Mark where platelets are.
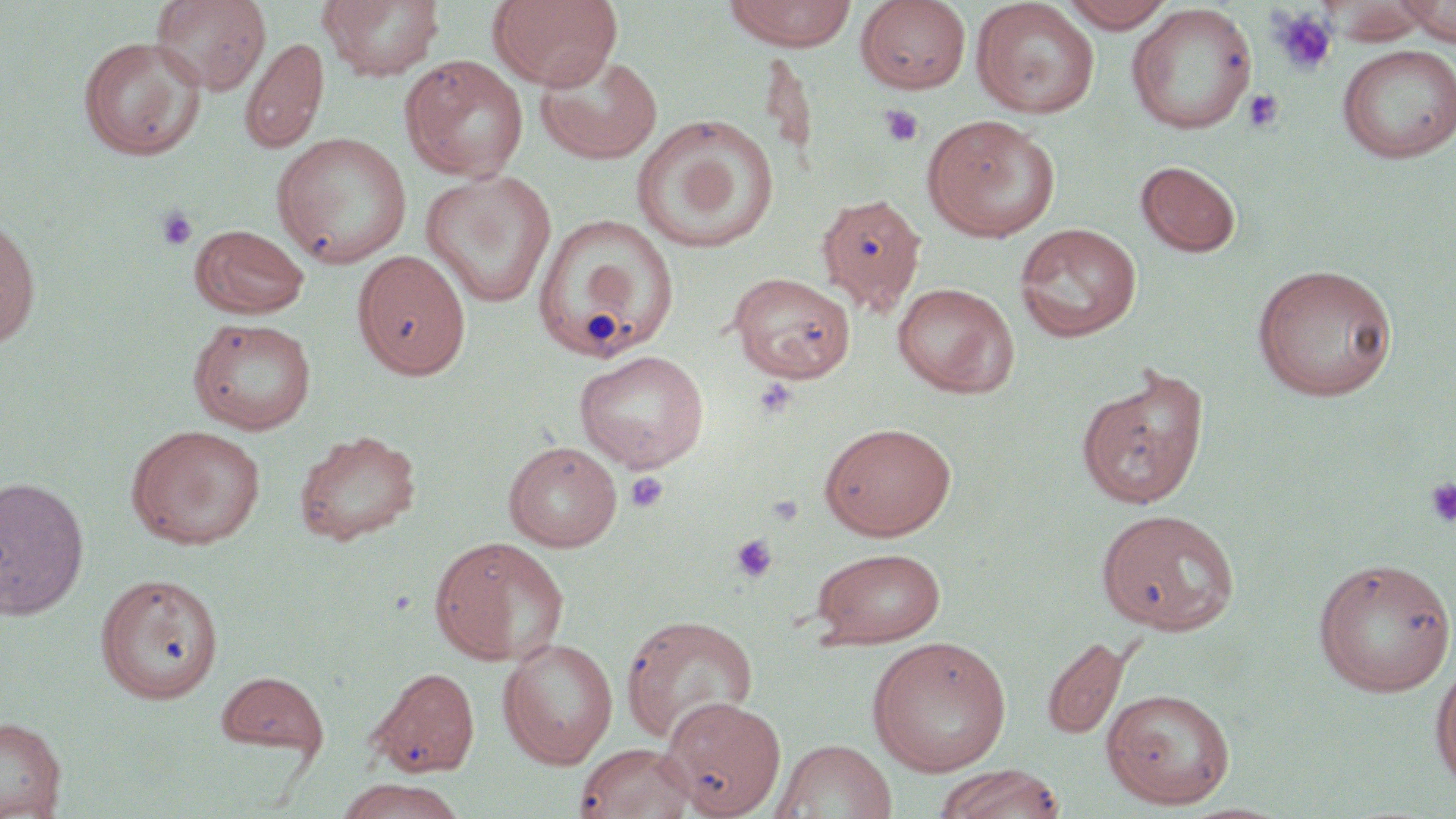
Approximate bounding boxes as (x1, y1, x2, y2) in pixels.
Platelets: (1270, 8, 1337, 75), (1242, 89, 1285, 132), (879, 104, 924, 148), (156, 205, 199, 251), (753, 377, 797, 419), (624, 471, 669, 513), (1424, 477, 1456, 527), (729, 533, 778, 584).

{
  "slide_level_diagnosis": "no evidence of blood parasites",
  "field_of_view": "single",
  "uninfected_red_blood_cell_locations": "approximate bounding boxes as (x1, y1, x2, y2) in pixels: (150, 0, 271, 94), (318, 0, 445, 82), (488, 0, 623, 91), (723, 0, 857, 50), (856, 0, 972, 94), (1058, 0, 1176, 32), (1398, 0, 1456, 46), (971, 1, 1100, 118), (1321, 1, 1431, 45), (1126, 3, 1257, 135), (78, 36, 206, 160), (239, 36, 329, 154), (1337, 45, 1455, 163), (760, 49, 818, 165), (534, 51, 663, 165), (399, 54, 529, 182), (632, 114, 780, 254), (922, 114, 1060, 242), (271, 132, 412, 269), (1136, 160, 1242, 258), (421, 169, 557, 308), (815, 192, 927, 316), (533, 214, 679, 362), (0, 215, 41, 351), (1014, 223, 1143, 342), (191, 224, 310, 318), (352, 250, 472, 380), (1251, 263, 1399, 402), (728, 271, 856, 383), (892, 281, 1019, 397), (188, 317, 317, 435), (573, 349, 710, 472), (1075, 366, 1211, 510), (819, 421, 957, 540), (126, 424, 267, 549), (294, 429, 422, 546), (503, 440, 622, 552), (0, 476, 90, 620), (1095, 508, 1240, 635), (429, 535, 569, 666), (810, 547, 947, 647), (1312, 556, 1456, 696), (95, 572, 225, 703), (620, 614, 758, 744), (1041, 635, 1129, 740), (867, 636, 1012, 776), (497, 637, 619, 769), (1430, 656, 1456, 791), (367, 666, 480, 776), (216, 671, 329, 758), (1100, 687, 1236, 809), (661, 695, 787, 818), (0, 717, 66, 817), (773, 738, 898, 818), (575, 741, 697, 819), (934, 763, 1066, 819), (334, 778, 466, 819)",
  "stain": "May-Grünwald-Giemsa",
  "preparation": "thin blood smear",
  "magnification": "1000x",
  "modality": "light microscopy",
  "image_size": "1456×819 pixels"
}